Describe the morphology of the red blood cells.
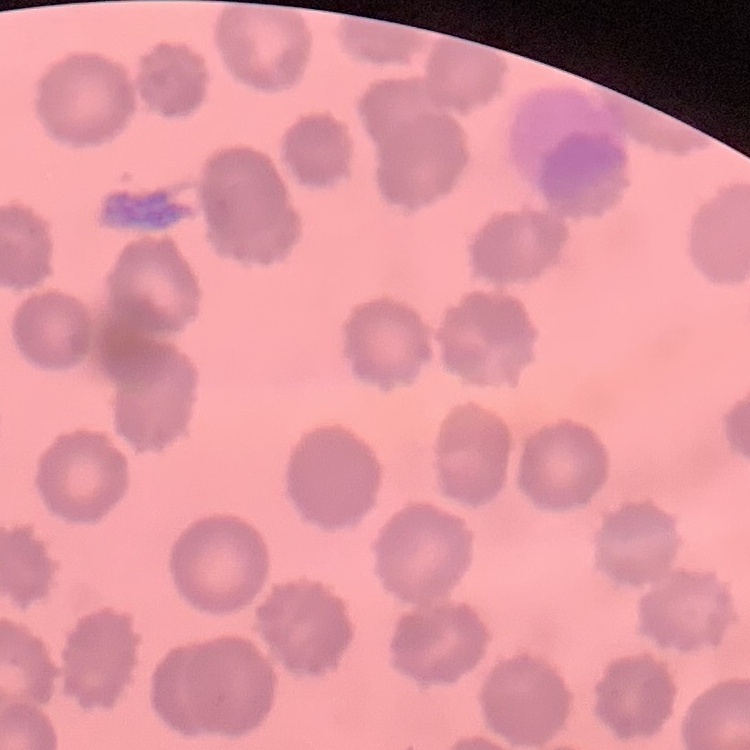
They show no rouleaux formation.

stain: Field's or Giemsa
preparation: thin peripheral smear
image_type: square crop of a larger photomicrograph